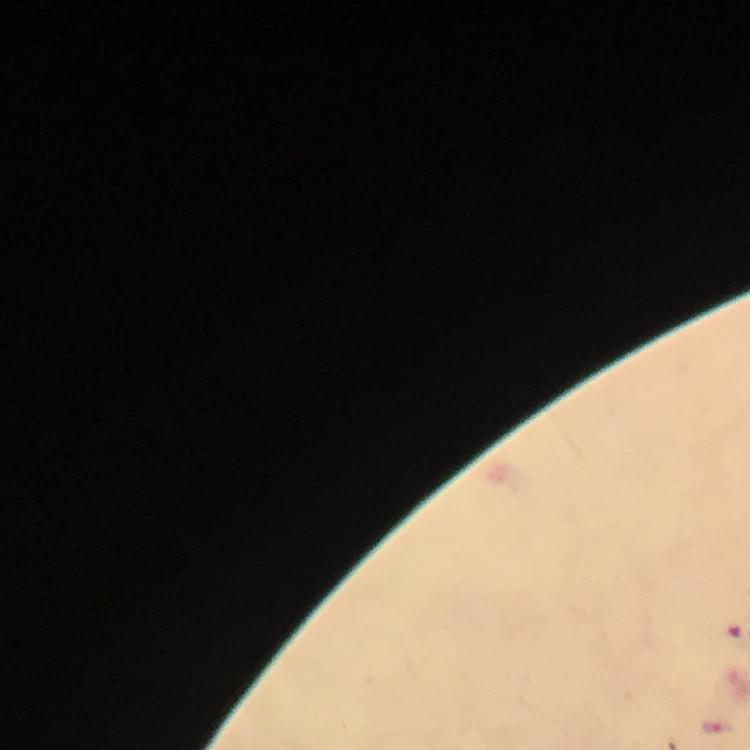
Approximate centers as [x, y] in pixels. Malaria parasite locations: [717, 725]. Thick blood smear. Image is 750×750 pixels. Photographed through the microscope with a smartphone camera. A crop from one field of view. Giemsa stain. At 100x magnification. From a malaria diagnostic workup. Immersion oil applied.